Locate malaria parasites and leukocytes.
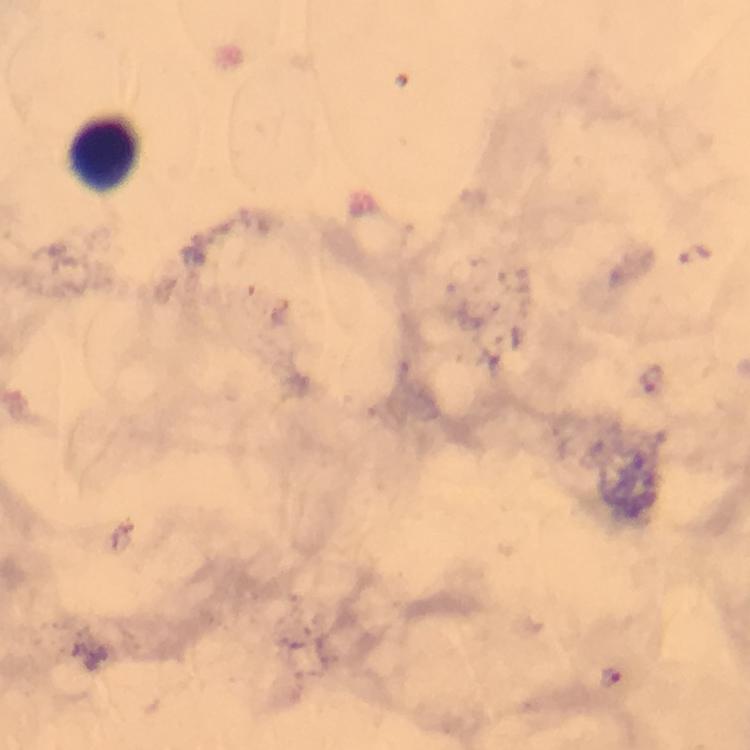
Approximate centers as [x, y] in pixels.
Malaria parasites: [697, 253], [653, 382], [607, 676].
Leukocytes: [101, 151].

Summary:
  - Immersion oil: used
  - Magnification: 100x
  - Stain: Giemsa
  - Image size: 750×750 pixels
  - Cropped from: one field of view
  - Context: from a malaria diagnostic workup
  - Capture: smartphone photograph through a microscope
  - Preparation: thick blood smear